Classify this cell by malaria status.
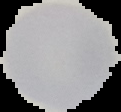
It is uninfected.

preparation: thin blood smear
image_size: 121×112 pixels
image_type: segmented cell region with the area outside set to black